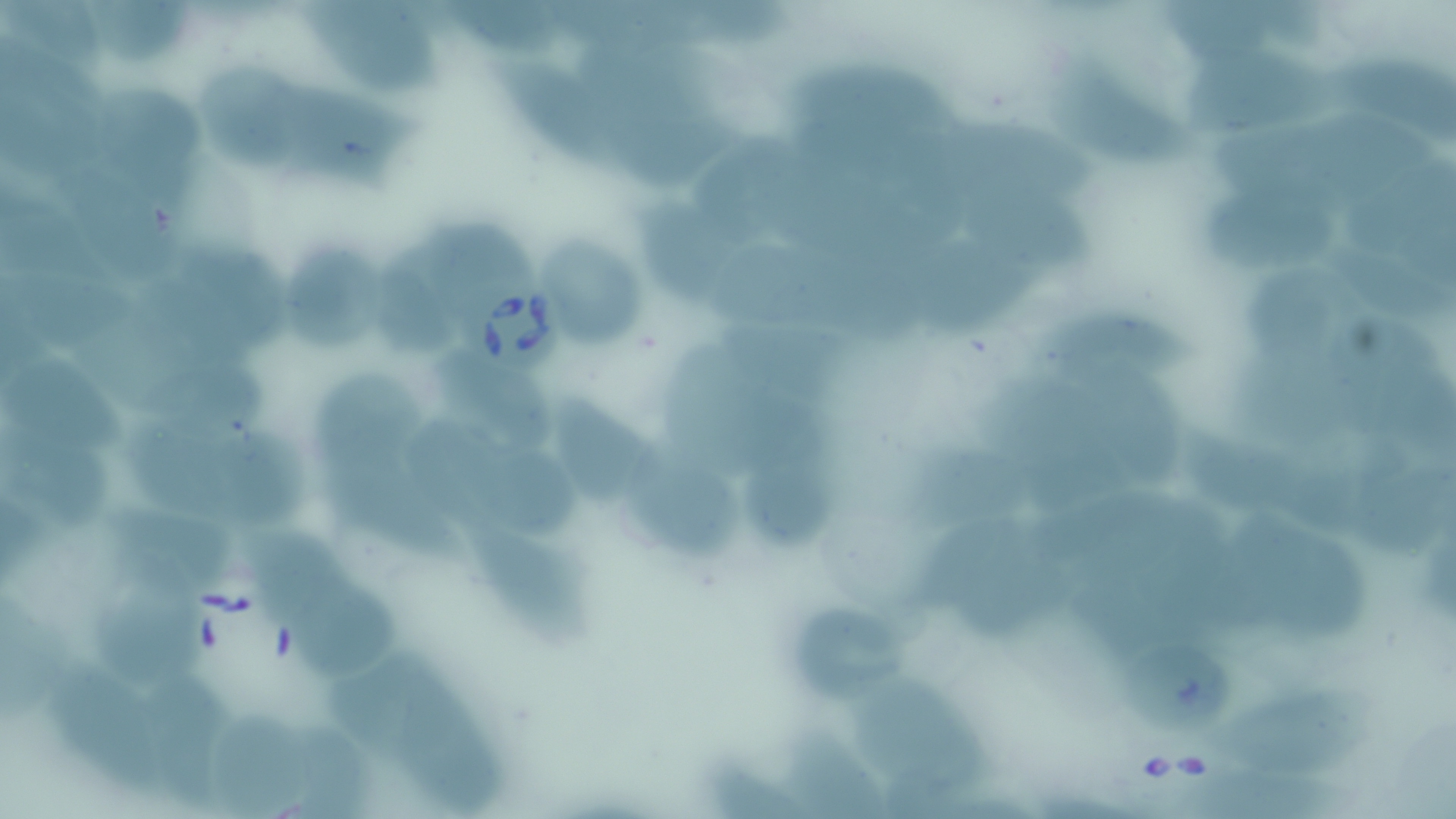
slide-level diagnosis = Babesia divergens
modality = light microscopy
preparation = thin blood smear
field of view = one of a larger specimen
magnification = 1000x
Babesia divergens-infected red blood cell locations = approximate bounding boxes as (x1,y1)-(x2,y2) corner pairs in pixels: (456,276)-(573,376)
image size = 1456×819 pixels
stain = May-Grünwald-Giemsa
uninfected red blood cell locations = approximate bounding boxes as (x1,y1)-(x2,y2) corner pairs in pixels: (440,0)-(574,66), (1161,0)-(1291,65), (1,2)-(113,74), (304,2)-(446,97), (87,4)-(192,71), (0,37)-(97,182), (587,43)-(733,188), (1048,46)-(1209,170), (1344,46)-(1456,145), (1180,49)-(1362,135), (493,55)-(634,178), (780,57)-(971,152), (192,58)-(312,171), (290,80)-(420,189), (75,84)-(208,194), (1211,111)-(1442,210), (696,124)-(813,254), (59,156)-(177,285), (962,176)-(1100,281), (1202,182)-(1337,280), (0,183)-(113,292), (630,194)-(745,303), (422,212)-(535,301), (278,232)-(398,359), (533,233)-(651,351), (376,238)-(461,365), (713,240)-(869,410), (1326,246)-(1456,327), (911,247)-(1037,338), (201,248)-(293,358), (1231,260)-(1371,368), (1044,309)-(1203,386), (1326,318)-(1456,434), (88,322)-(274,433), (665,338)-(768,472), (2,349)-(131,452), (1228,352)-(1389,459), (440,353)-(557,454), (1093,355)-(1192,497), (314,369)-(419,477), (548,394)-(658,512), (209,416)-(313,529), (123,419)-(244,515), (411,420)-(523,533), (3,431)-(121,527), (464,438)-(584,544), (620,441)-(742,565), (919,445)-(1024,520), (742,451)-(831,549), (1346,455)-(1456,562), (325,466)-(470,563), (1230,496)-(1377,647), (108,500)-(236,594), (467,517)-(589,640), (919,521)-(1074,644), (246,524)-(352,620), (88,577)-(205,688), (286,577)-(405,685), (1,591)-(65,743), (781,595)-(908,707), (1118,635)-(1234,737), (325,640)-(430,768), (53,657)-(168,795), (143,666)-(243,800), (397,672)-(515,813), (850,672)-(992,796), (1210,686)-(1378,781), (200,708)-(318,817), (779,724)-(890,819), (1169,759)-(1336,819), (707,760)-(808,819)